Assess this cell for malaria.
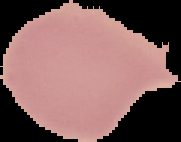
Uninfected.

The area outside the segmented cell region is set to black. From a thin blood smear. Image is 181×142 pixels.